Comment on the morphology of the erythrocytes.
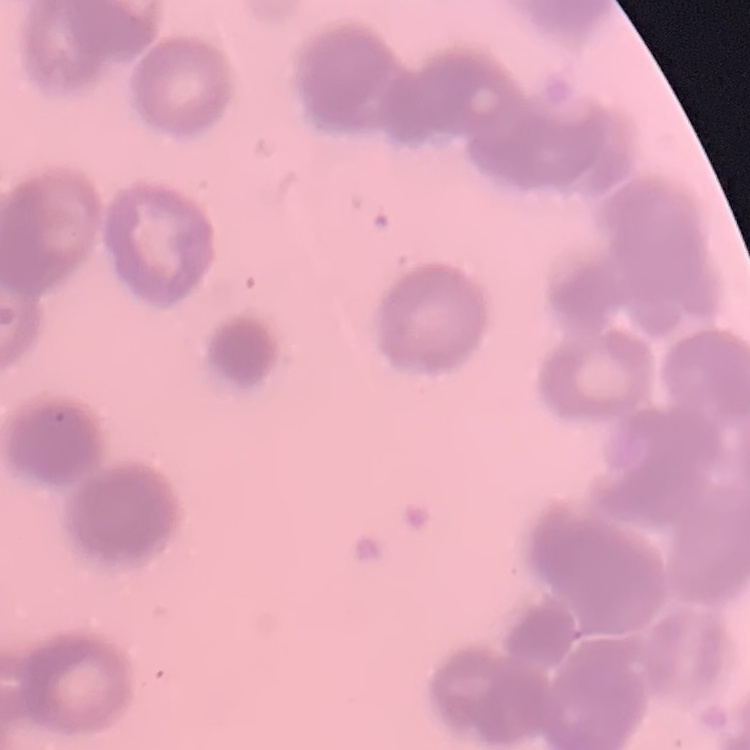
They show rouleaux formation.

stain = Field's or Giemsa
preparation = thin peripheral smear
image type = one tile cut from a larger photomicrograph